State which parasite is depicted.
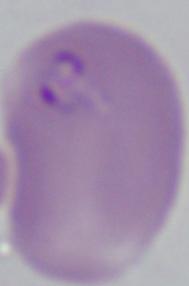

This is Babesia.

Summary:
  - Magnification: 1000x
  - Modality: photomicrograph